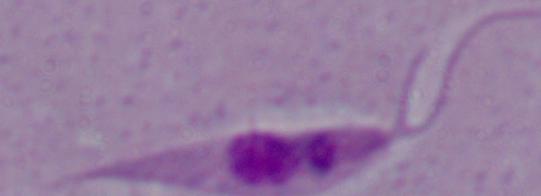 A Leishmania parasite is shown. Captured at 1000x magnification. Photomicrograph.